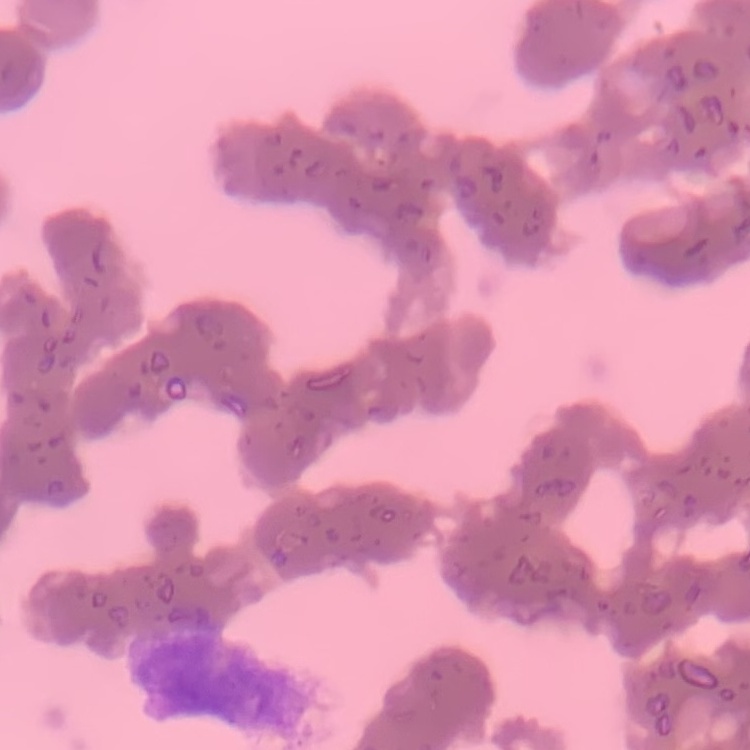
The erythrocytes exhibit rouleaux formation. Thin peripheral smear. One tile cut from a larger photomicrograph. Field's or Giemsa stain.